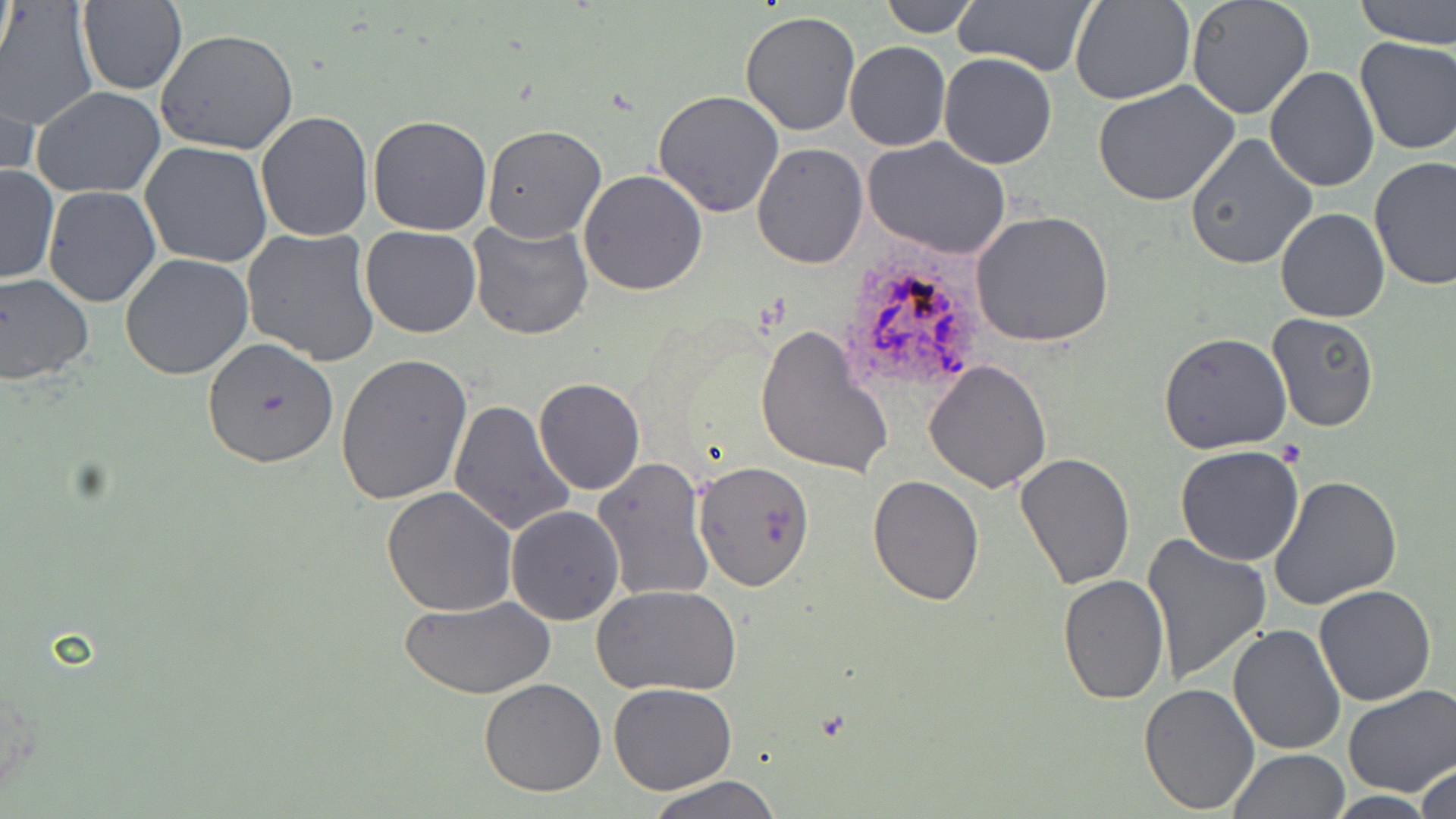

Summary:
  - Coordinate format: approximate bounding boxes as named x1/y1/x2/y2 corners in pixels
  - Uninfected red blood cell locations: (x1=878, y1=0, x2=980, y2=37), (x1=953, y1=0, x2=1097, y2=77), (x1=1070, y1=0, x2=1195, y2=105), (x1=1185, y1=0, x2=1314, y2=119), (x1=1354, y1=0, x2=1456, y2=47), (x1=77, y1=2, x2=185, y2=94), (x1=1, y1=3, x2=96, y2=133), (x1=739, y1=9, x2=862, y2=137), (x1=156, y1=27, x2=299, y2=156), (x1=1355, y1=36, x2=1455, y2=155), (x1=844, y1=41, x2=951, y2=151), (x1=940, y1=54, x2=1057, y2=169), (x1=1, y1=68, x2=37, y2=187), (x1=1265, y1=68, x2=1378, y2=193), (x1=1095, y1=81, x2=1240, y2=208), (x1=30, y1=86, x2=167, y2=198), (x1=653, y1=90, x2=785, y2=218), (x1=255, y1=112, x2=375, y2=243), (x1=367, y1=116, x2=493, y2=236), (x1=481, y1=125, x2=606, y2=243), (x1=1184, y1=133, x2=1318, y2=270), (x1=864, y1=136, x2=1011, y2=260), (x1=140, y1=142, x2=273, y2=268), (x1=751, y1=143, x2=867, y2=267), (x1=1369, y1=156, x2=1455, y2=291), (x1=0, y1=164, x2=58, y2=285), (x1=578, y1=170, x2=707, y2=296), (x1=43, y1=186, x2=161, y2=308), (x1=1276, y1=208, x2=1389, y2=322), (x1=971, y1=209, x2=1114, y2=347), (x1=468, y1=219, x2=595, y2=341), (x1=360, y1=225, x2=482, y2=340), (x1=241, y1=227, x2=380, y2=366), (x1=120, y1=254, x2=254, y2=378), (x1=0, y1=272, x2=94, y2=385), (x1=1266, y1=313, x2=1379, y2=431), (x1=755, y1=327, x2=894, y2=482), (x1=1158, y1=332, x2=1292, y2=454), (x1=201, y1=338, x2=340, y2=468), (x1=335, y1=353, x2=473, y2=506), (x1=924, y1=359, x2=1052, y2=493), (x1=534, y1=378, x2=645, y2=495), (x1=450, y1=399, x2=576, y2=538), (x1=1175, y1=446, x2=1306, y2=566), (x1=1014, y1=452, x2=1135, y2=589), (x1=592, y1=457, x2=714, y2=604), (x1=695, y1=461, x2=817, y2=592), (x1=865, y1=475, x2=985, y2=606), (x1=1269, y1=475, x2=1405, y2=611), (x1=382, y1=485, x2=517, y2=616), (x1=505, y1=504, x2=624, y2=625), (x1=1140, y1=531, x2=1272, y2=688), (x1=1058, y1=574, x2=1169, y2=704), (x1=592, y1=583, x2=741, y2=696), (x1=1314, y1=583, x2=1437, y2=705), (x1=402, y1=595, x2=558, y2=700), (x1=1227, y1=623, x2=1346, y2=756), (x1=478, y1=678, x2=607, y2=797), (x1=1138, y1=681, x2=1260, y2=814), (x1=609, y1=682, x2=737, y2=794), (x1=1342, y1=687, x2=1455, y2=796), (x1=1228, y1=749, x2=1348, y2=819), (x1=1414, y1=759, x2=1456, y2=819), (x1=645, y1=776, x2=782, y2=818)
  - Plasmodium ovale-infected red blood cell locations: (x1=833, y1=253, x2=988, y2=395)
  - Slide-level diagnosis: Plasmodium ovale
  - Modality: optical microscopy
  - Stain: May-Grünwald-Giemsa
  - Image size: 1456×819 pixels
  - Magnification: 1000x
  - Field of view: single
  - Preparation: thin blood smear